Outline each Plasmodium ovale-infected red blood cell.
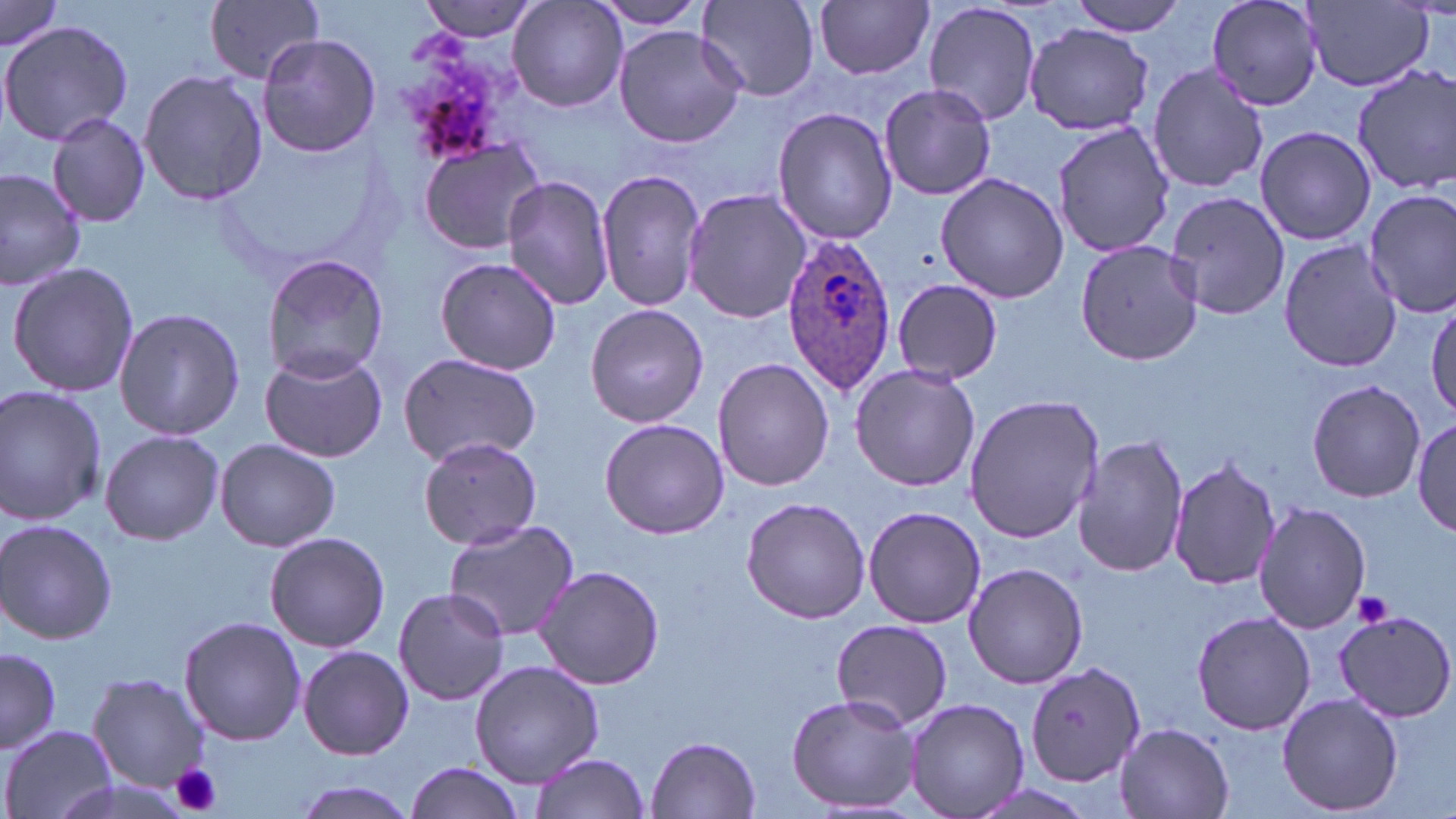
Approximate bounding boxes as [x1, y1, x2, y2] in pixels.
Plasmodium ovale-infected red blood cells: [782, 231, 897, 395].

Platelet locations: [1352, 590, 1393, 627], [171, 762, 224, 817]. Uninfected red blood cell locations: [202, 0, 326, 85], [420, 0, 539, 45], [507, 0, 627, 114], [587, 0, 711, 29], [699, 0, 820, 102], [1065, 0, 1190, 34], [1207, 0, 1324, 112], [816, 1, 933, 80], [923, 1, 1044, 127], [1301, 1, 1435, 91], [0, 2, 65, 56], [0, 19, 134, 145], [1023, 23, 1155, 134], [613, 25, 747, 150], [257, 32, 380, 158], [1147, 63, 1270, 195], [1350, 63, 1456, 195], [139, 67, 268, 208], [877, 83, 997, 201], [773, 106, 899, 246], [45, 111, 150, 228], [1052, 123, 1172, 261], [1255, 126, 1376, 245], [417, 136, 548, 255], [597, 167, 706, 311], [0, 169, 85, 289], [936, 171, 1070, 303], [501, 175, 616, 310], [1363, 187, 1456, 319], [682, 188, 813, 324], [1165, 191, 1288, 321], [1278, 238, 1401, 375], [1075, 240, 1203, 366], [261, 253, 389, 383], [435, 256, 562, 376], [6, 262, 140, 399], [893, 279, 1004, 384], [1428, 299, 1456, 419], [584, 303, 709, 428], [113, 307, 245, 441], [258, 349, 387, 461], [394, 353, 543, 467], [712, 357, 835, 490], [850, 364, 982, 493], [1307, 380, 1425, 502], [0, 385, 107, 524], [963, 394, 1103, 545], [600, 417, 731, 538], [1413, 417, 1455, 535], [101, 429, 225, 545], [1073, 433, 1188, 580], [417, 435, 543, 549], [216, 438, 341, 552], [1169, 456, 1280, 592], [741, 497, 871, 624], [1253, 500, 1371, 632], [862, 504, 986, 628], [0, 518, 118, 646], [445, 519, 580, 643], [263, 532, 392, 652], [962, 560, 1089, 688], [537, 565, 664, 689], [392, 589, 510, 706], [1190, 609, 1316, 734], [1332, 611, 1455, 723], [179, 616, 306, 746], [829, 618, 955, 730], [299, 644, 413, 760], [1, 648, 59, 755], [1024, 660, 1146, 788], [470, 661, 603, 787], [86, 671, 210, 794], [1277, 692, 1403, 815], [786, 693, 920, 813], [905, 698, 1029, 818], [1113, 722, 1234, 819], [3, 724, 115, 819], [647, 736, 760, 817], [528, 753, 651, 818], [404, 761, 525, 819], [291, 779, 415, 819]. Slide-level diagnosis: Plasmodium ovale. Single field of view. Light microscopy. Image is 1456×819 pixels. Thin blood film. Captured at 1000x magnification. May-Grünwald-Giemsa-stained preparation.